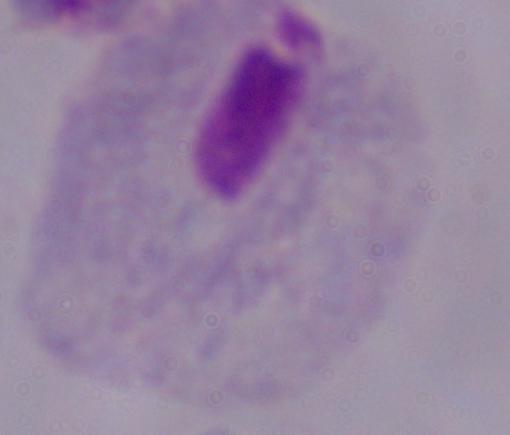
Captured at 1000x magnification. Micrograph. A trichomonad is seen.